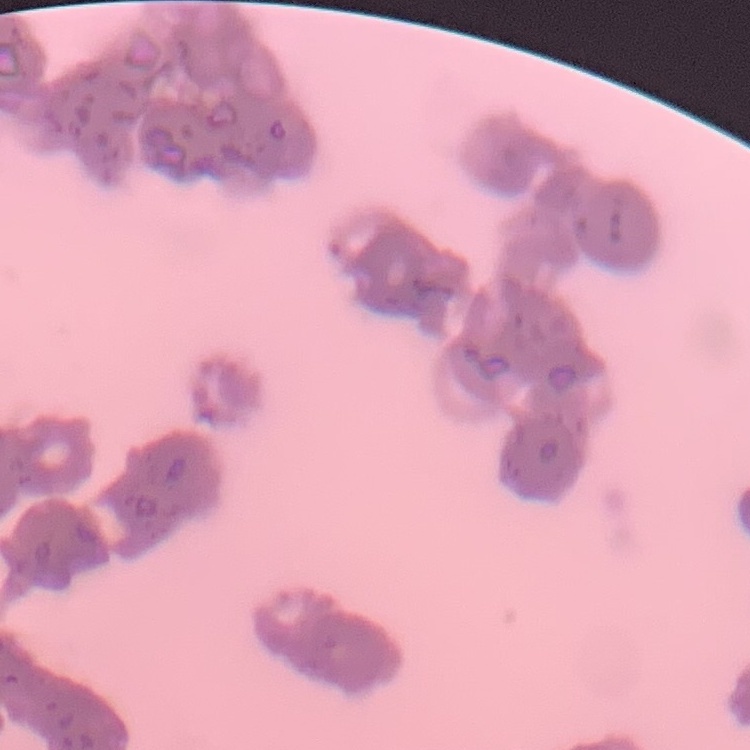

erythrocyte morphology = rouleaux formation
preparation = thin blood smear
stain = Field's or Giemsa
image type = one tile cut from a larger photomicrograph